Name the parasite shown.
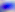

Toxoplasma gondii.

Photomicrograph. 400x magnification.